Outline each blood parasite and name the species.
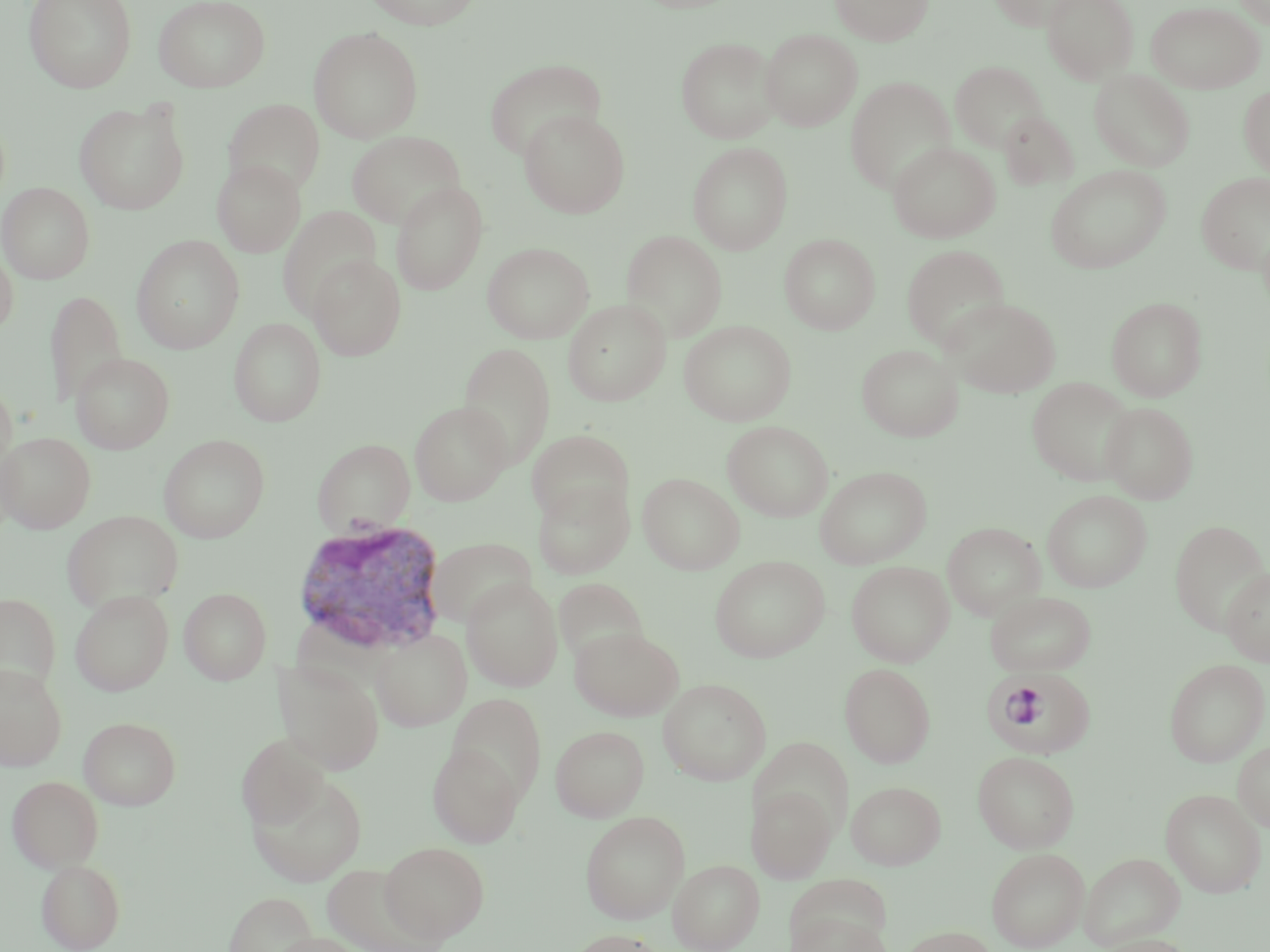
Approximate bounding boxes as [x1, y1, x2, y2] in pixels.
Plasmodium vivax-infected red blood cells: [290, 518, 449, 656], [980, 670, 1100, 755].
No Plasmodium falciparum, Plasmodium ovale, Plasmodium malariae, Babesia divergens, or Trypanosoma brucei observed.

slide-level diagnosis = Plasmodium vivax
field of view = one of a larger specimen
magnification = 1000x
preparation = thin blood film
stain = May-Grünwald-Giemsa
image size = 1270×952 pixels
uninfected red blood cell locations = approximate bounding boxes as [x1, y1, x2, y2] in pixels: [24, 0, 136, 92], [153, 0, 270, 92], [363, 0, 483, 29], [831, 0, 934, 45], [987, 0, 1086, 31], [1042, 0, 1138, 83], [1232, 0, 1270, 28], [1145, 1, 1266, 93], [308, 26, 424, 143], [761, 29, 862, 131], [675, 36, 781, 143], [484, 59, 607, 161], [950, 60, 1048, 152], [1089, 69, 1195, 172], [845, 77, 956, 194], [1238, 84, 1270, 178], [223, 98, 325, 198], [74, 99, 190, 214], [518, 109, 630, 218], [998, 109, 1080, 191], [347, 130, 466, 230], [888, 141, 1000, 243], [688, 142, 793, 254], [213, 159, 306, 257], [1045, 166, 1171, 273], [1196, 172, 1270, 275], [390, 181, 487, 295], [0, 182, 95, 284], [276, 206, 383, 318], [621, 230, 728, 341], [779, 233, 880, 334], [131, 235, 245, 353], [482, 241, 594, 343], [0, 242, 18, 338], [901, 244, 1010, 350], [308, 255, 406, 361], [44, 289, 127, 409], [1107, 296, 1207, 401], [943, 297, 1061, 397], [563, 299, 670, 405], [229, 317, 326, 427], [680, 320, 796, 426], [457, 342, 556, 470], [856, 343, 963, 442], [71, 352, 174, 453], [1027, 377, 1136, 485], [0, 380, 17, 479], [409, 401, 511, 505], [1101, 402, 1198, 504], [722, 420, 834, 521], [527, 429, 634, 526], [0, 432, 95, 533], [159, 434, 270, 543], [312, 438, 415, 536], [815, 466, 931, 568], [638, 473, 744, 574], [532, 480, 634, 579], [1042, 490, 1152, 592], [62, 510, 183, 613], [1170, 520, 1269, 633], [942, 522, 1045, 620], [427, 537, 537, 630], [710, 556, 829, 662], [846, 561, 954, 667], [1221, 567, 1270, 667], [554, 577, 647, 668], [462, 578, 563, 692], [179, 587, 271, 685], [70, 589, 173, 696], [986, 591, 1096, 675], [0, 593, 60, 697], [570, 626, 683, 720], [372, 629, 471, 731], [1164, 659, 1269, 766], [273, 662, 384, 774], [840, 663, 936, 767], [0, 664, 67, 770], [658, 679, 771, 785], [447, 693, 547, 804], [78, 716, 181, 810], [551, 724, 649, 821], [236, 735, 330, 828], [750, 739, 852, 840], [1233, 740, 1270, 831], [427, 743, 523, 847], [973, 751, 1080, 853], [247, 772, 368, 887], [7, 775, 104, 872], [847, 780, 946, 869], [746, 785, 836, 882], [1160, 788, 1267, 897], [580, 810, 689, 924], [380, 841, 490, 942], [987, 847, 1089, 951], [1079, 852, 1185, 950], [36, 859, 126, 951], [669, 860, 764, 951], [322, 863, 448, 951], [223, 891, 319, 952], [788, 912, 892, 952], [897, 925, 999, 952], [567, 929, 668, 952], [269, 932, 369, 952], [1092, 934, 1196, 952]
modality = light microscopy